Locate every Plasmodium falciparum-infected red blood cell.
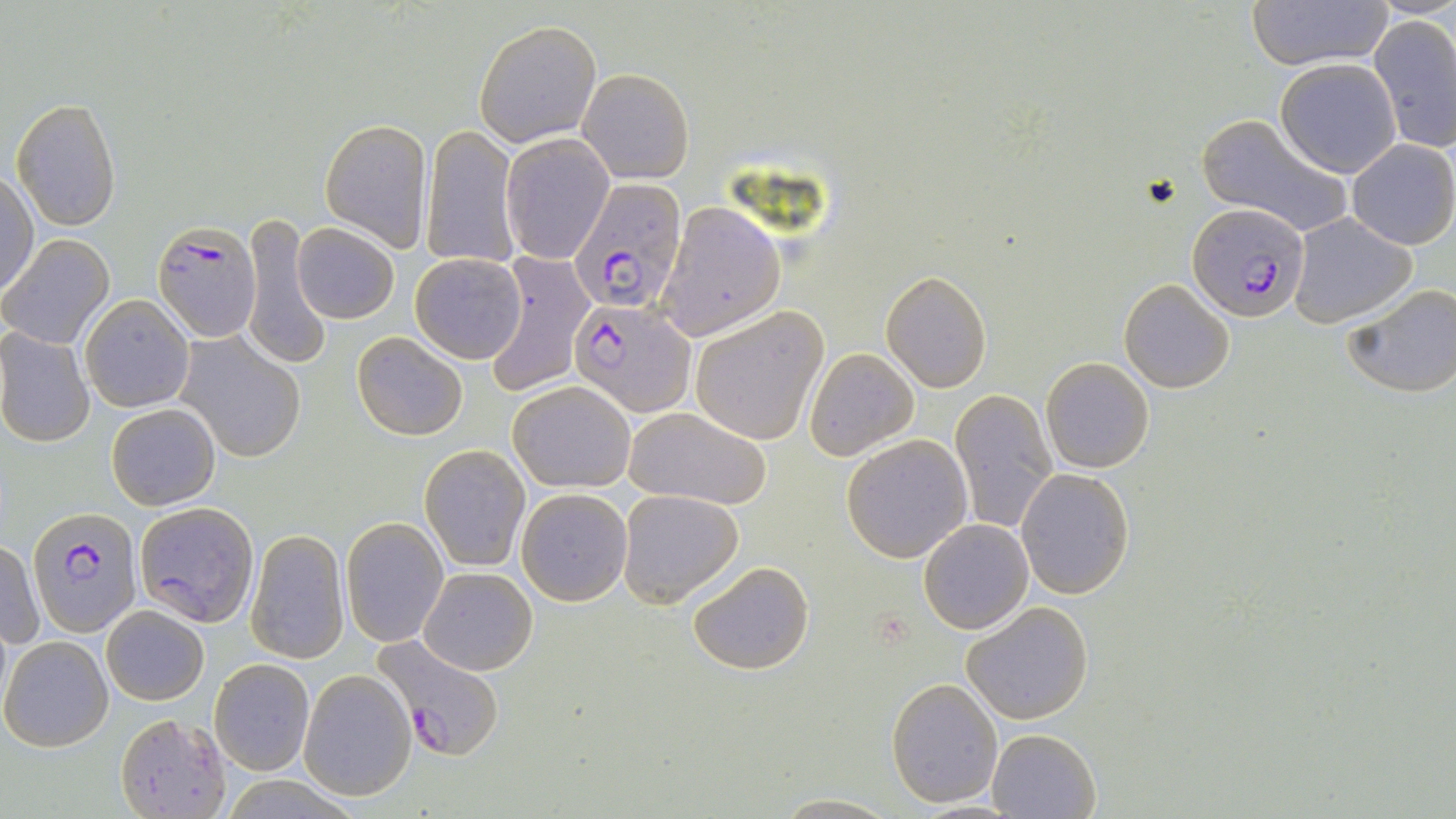

Approximate bounding boxes as [x1, y1, x2, y2] in pixels.
Plasmodium falciparum-infected red blood cells: [569, 176, 687, 315], [1187, 202, 1310, 323], [154, 219, 260, 342], [571, 299, 696, 416], [28, 505, 138, 639], [373, 633, 505, 759].

slide-level diagnosis = Plasmodium falciparum
field of view = single
uninfected red blood cell locations = approximate bounding boxes as [x1, y1, x2, y2] in pixels: [1249, 0, 1390, 70], [1369, 15, 1456, 153], [474, 20, 602, 147], [1273, 59, 1402, 178], [579, 67, 695, 183], [12, 97, 123, 231], [1196, 112, 1352, 238], [319, 118, 432, 251], [422, 126, 518, 270], [501, 134, 612, 264], [1347, 139, 1456, 249], [0, 173, 38, 299], [654, 203, 786, 339], [238, 211, 331, 372], [1288, 213, 1417, 328], [291, 222, 399, 324], [1, 235, 114, 349], [410, 251, 527, 363], [485, 255, 593, 396], [881, 272, 992, 392], [1118, 278, 1234, 393], [1344, 282, 1456, 398], [81, 294, 195, 411], [690, 308, 827, 444], [0, 327, 95, 449], [352, 330, 468, 441], [177, 332, 306, 461], [805, 347, 918, 460], [1040, 356, 1154, 473], [507, 379, 637, 493], [949, 387, 1059, 537], [106, 402, 219, 511], [623, 405, 774, 511], [841, 435, 973, 563], [420, 443, 530, 571], [1016, 468, 1135, 600], [516, 488, 632, 605], [617, 489, 744, 606], [135, 500, 260, 626], [341, 516, 448, 647], [919, 519, 1034, 634], [246, 528, 349, 664], [1, 539, 42, 652], [687, 561, 813, 676], [421, 566, 537, 675], [960, 600, 1096, 724], [101, 605, 208, 705], [1, 636, 114, 752], [209, 658, 314, 775], [298, 670, 416, 802], [886, 676, 1002, 807], [116, 711, 232, 818], [988, 727, 1100, 818], [770, 794, 900, 818]
preparation = thin blood film
modality = light microscopy
image size = 1456×819 pixels
stain = May-Grünwald-Giemsa
magnification = 1000x